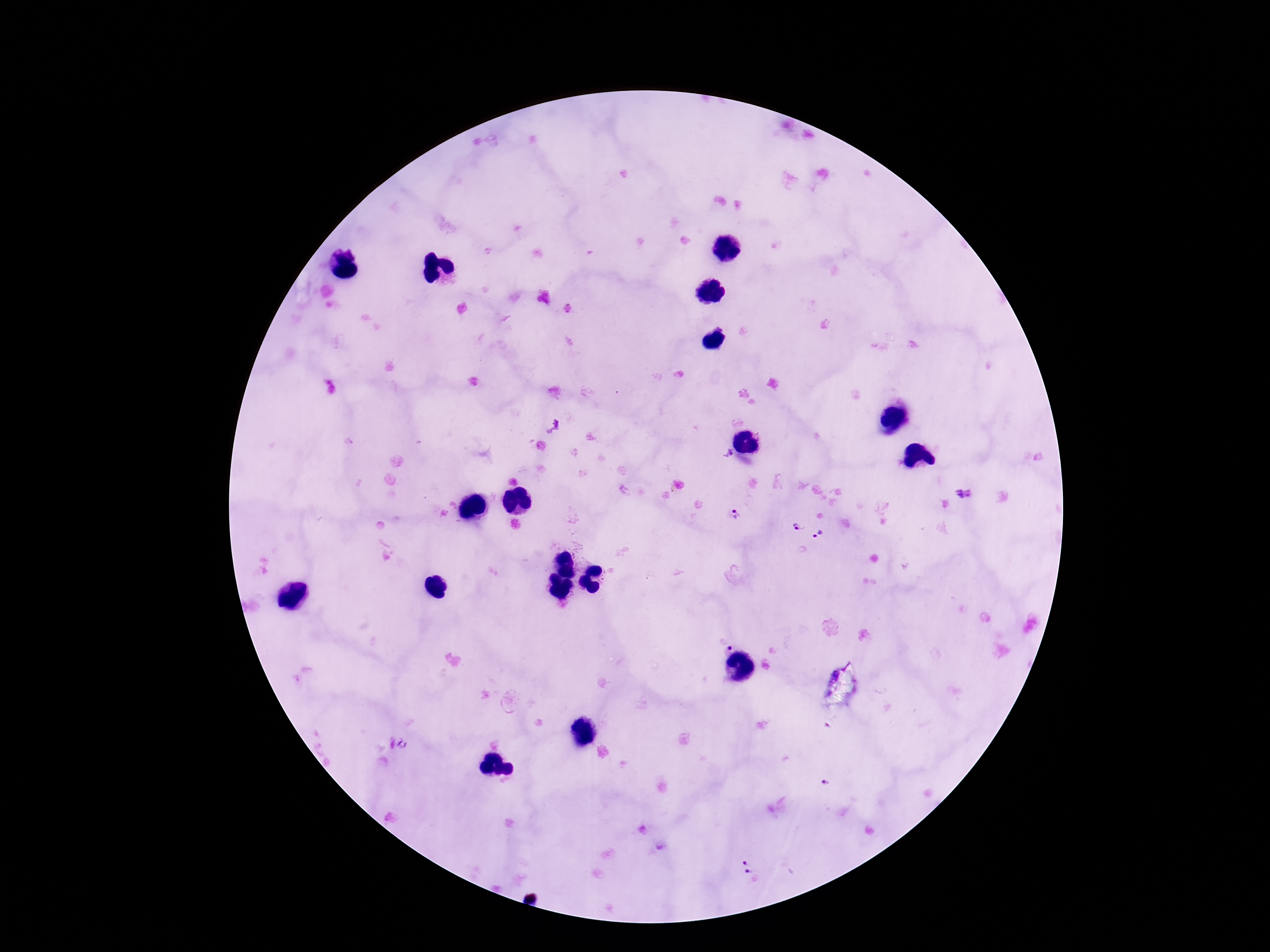
Approximate object centers, in pixels from the top-left corner. Plasmodium parasite locations: (x=725, y=454), (x=965, y=493), (x=732, y=513), (x=797, y=529), (x=822, y=537), (x=724, y=642), (x=825, y=783), (x=750, y=870). Patient malaria status: positive. Thick blood smear. Photographed through the microscope eyepiece with a smartphone camera. Image is 1270×952 pixels. One field from this slide. Giemsa stain. 100x magnification.